Classify this cell by malaria status.
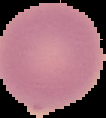

It is uninfected.

image type = segmented cell region on a black background
image size = 106×118 pixels
preparation = thin blood film